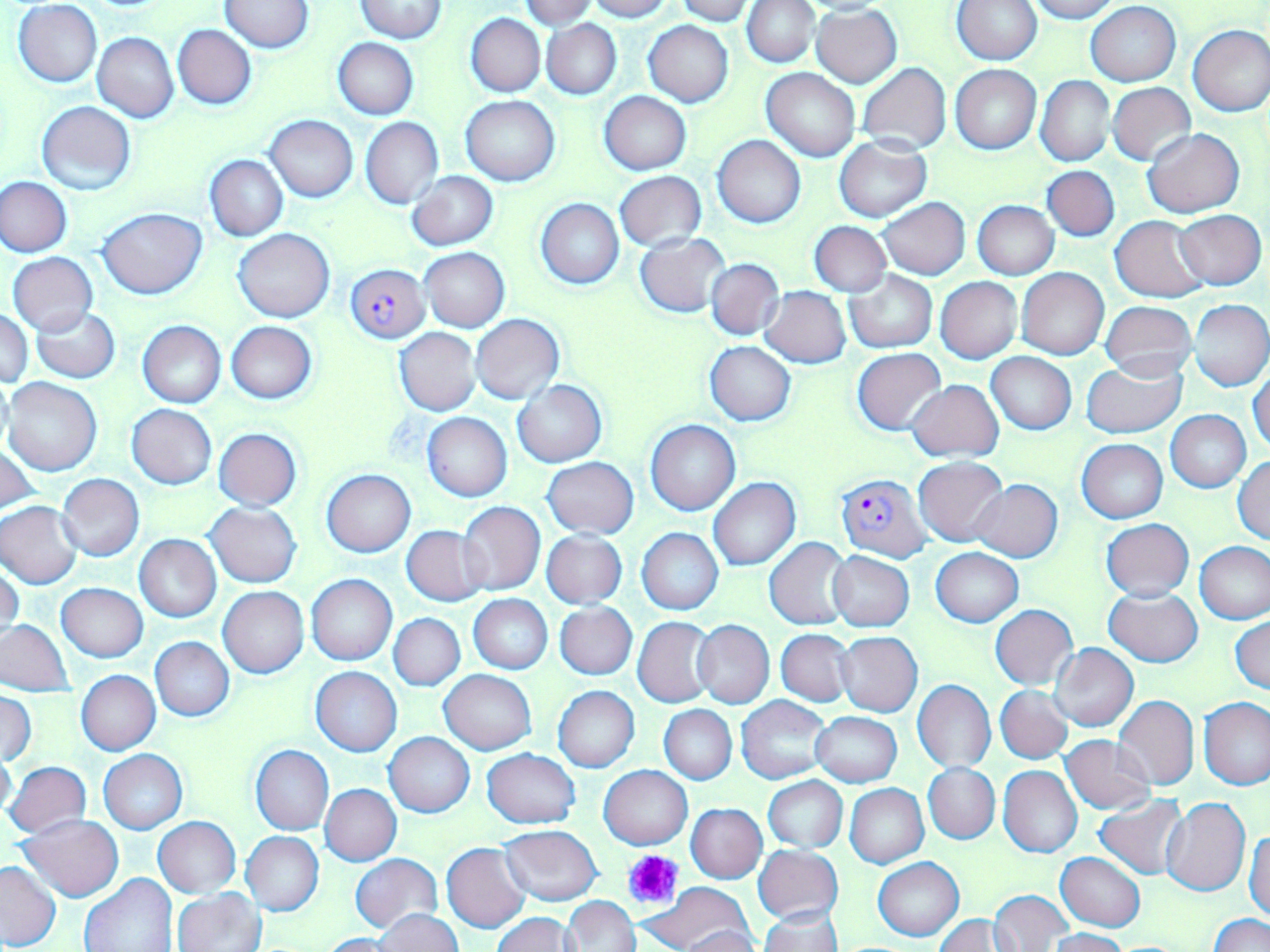
Summary:
  - Coordinate format: approximate bounding boxes as (x1, y1, x2, y2) in pixels
  - Plasmodium falciparum-infected red blood cell locations: (346, 264, 430, 343), (836, 472, 932, 562)
  - Uninfected red blood cell locations: (522, 0, 597, 29), (585, 0, 672, 21), (677, 0, 756, 25), (742, 0, 818, 68), (953, 0, 1042, 65), (1025, 0, 1119, 23), (13, 1, 102, 87), (220, 1, 315, 51), (354, 1, 447, 42), (1086, 2, 1180, 85), (811, 7, 902, 87), (466, 13, 545, 97), (542, 20, 621, 98), (642, 21, 732, 107), (1187, 24, 1270, 116), (172, 25, 256, 109), (93, 32, 179, 122), (333, 37, 418, 120), (857, 62, 951, 154), (950, 64, 1040, 154), (761, 68, 861, 162), (1036, 75, 1115, 167), (1108, 83, 1195, 166), (600, 92, 691, 174), (461, 94, 559, 184), (36, 100, 137, 195), (265, 115, 358, 201), (360, 117, 443, 209), (1143, 128, 1244, 218), (713, 136, 806, 227), (835, 137, 932, 223), (205, 154, 288, 241), (1043, 166, 1118, 242), (407, 171, 498, 250), (614, 171, 706, 250), (1, 176, 72, 257), (878, 198, 970, 280), (536, 199, 624, 289), (973, 200, 1058, 279), (97, 207, 207, 297), (1174, 211, 1266, 289), (1110, 216, 1209, 303), (809, 221, 891, 296), (233, 229, 334, 321), (635, 232, 732, 318), (421, 247, 509, 332), (7, 252, 98, 336), (706, 258, 785, 341), (1016, 268, 1109, 359), (844, 269, 938, 353), (936, 277, 1022, 364), (760, 285, 850, 367), (1100, 300, 1196, 379), (1189, 300, 1270, 391), (31, 307, 120, 382), (1, 309, 33, 388), (471, 313, 564, 404), (137, 321, 225, 408), (226, 321, 317, 404), (394, 328, 481, 415), (705, 341, 796, 425), (852, 347, 945, 437), (986, 352, 1077, 435), (1081, 360, 1187, 438), (1249, 368, 1270, 455), (3, 377, 102, 476), (907, 379, 1004, 462), (513, 380, 606, 467), (127, 404, 216, 488), (1166, 410, 1251, 493), (422, 412, 512, 502), (645, 419, 740, 516), (213, 428, 302, 510), (1077, 438, 1167, 523), (1, 444, 40, 516), (1233, 455, 1270, 544), (914, 457, 1008, 546), (542, 458, 638, 538), (322, 469, 415, 557), (57, 474, 144, 561), (708, 478, 801, 571), (973, 479, 1063, 563), (204, 501, 301, 587), (457, 501, 545, 597), (0, 502, 84, 589), (1101, 519, 1194, 601), (402, 525, 491, 607), (637, 528, 723, 614), (541, 531, 627, 607), (135, 534, 222, 622), (764, 537, 853, 630), (1195, 542, 1270, 623), (932, 547, 1023, 627), (829, 551, 914, 631), (1, 565, 23, 643), (306, 574, 397, 665), (57, 583, 148, 661), (218, 587, 309, 677), (1104, 588, 1203, 666), (470, 595, 552, 673), (555, 602, 638, 679), (990, 605, 1078, 689), (389, 613, 465, 691), (1231, 614, 1270, 694), (633, 617, 716, 706), (0, 619, 74, 696), (694, 621, 774, 708), (776, 629, 855, 706), (835, 631, 922, 716), (150, 637, 234, 721), (1049, 643, 1137, 732), (310, 666, 401, 756), (76, 670, 160, 755), (439, 670, 537, 754), (913, 680, 996, 771), (996, 685, 1074, 764), (552, 686, 639, 773), (0, 691, 36, 767), (736, 695, 831, 785), (1112, 695, 1199, 790), (1200, 698, 1270, 789), (660, 705, 736, 784), (810, 712, 901, 787), (384, 731, 475, 817), (1061, 735, 1154, 814), (0, 743, 17, 823), (250, 745, 334, 835), (482, 747, 580, 829), (99, 750, 188, 834), (5, 761, 90, 837), (924, 762, 1000, 844), (599, 765, 692, 849), (998, 766, 1083, 858), (764, 776, 847, 853), (845, 783, 928, 869), (320, 784, 401, 865), (1094, 796, 1189, 880), (1162, 798, 1251, 896), (686, 803, 766, 883), (18, 815, 124, 901), (152, 817, 240, 898), (498, 826, 603, 905), (1246, 826, 1270, 922), (240, 831, 323, 916), (442, 842, 530, 932), (754, 845, 842, 925), (1056, 852, 1145, 931), (351, 853, 441, 932), (872, 857, 963, 940), (0, 861, 61, 950), (79, 872, 177, 952), (647, 883, 755, 951), (170, 889, 265, 952), (989, 889, 1073, 951), (560, 895, 642, 952), (758, 907, 842, 952), (376, 909, 462, 951), (1207, 913, 1269, 952), (494, 914, 577, 952), (931, 915, 1009, 951), (1007, 916, 1108, 951), (679, 927, 764, 952), (1048, 928, 1129, 952), (320, 934, 399, 952)
  - Platelet locations: (622, 849, 684, 910)
  - Slide-level diagnosis: Plasmodium falciparum
  - Stain: May-Grünwald-Giemsa
  - Field of view: single
  - Image size: 1270×952 pixels
  - Magnification: 1000x
  - Modality: optical microscopy
  - Preparation: thin blood film